Classify this cell by malaria status.
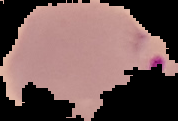

Parasitized.

Cell region segmented out of the field of view; the surrounding area is masked to black. From a thin blood smear. Image is 178×121 pixels.